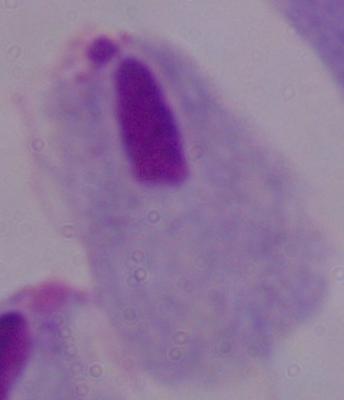
Summary:
  - Identification: trichomonad
  - Modality: photomicrograph
  - Magnification: 1000x